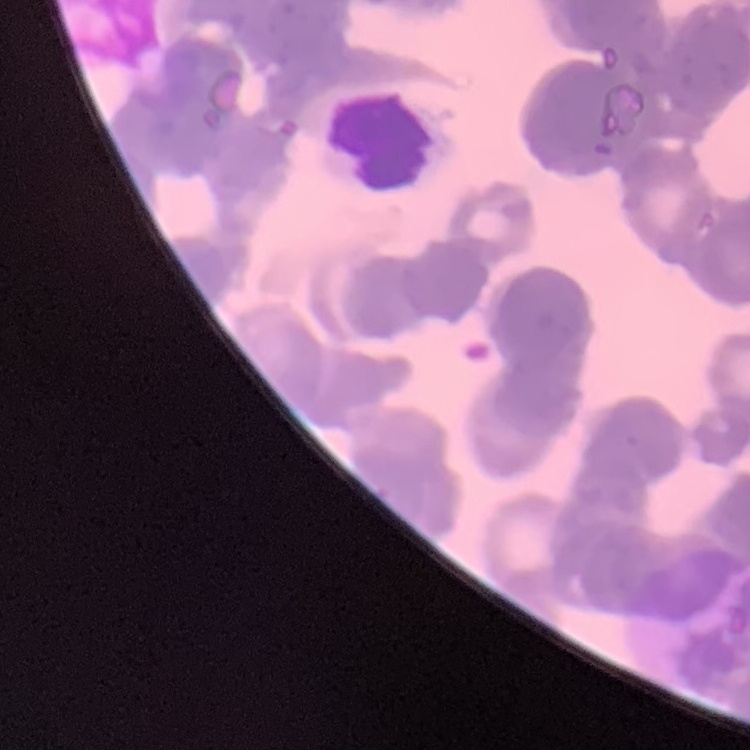 The red blood cells show rouleaux formation. Square crop of a larger photomicrograph. Thin blood smear. Stained with either Field's or Giemsa.